Name the parasite shown.
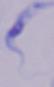

This is a trypanosome.

modality = photomicrograph
magnification = 1000x